Report the malaria status of this cell.
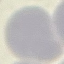

It is uninfected.

Summary:
  - Image type: automatically extracted cell patch, resized to 64 × 64 pixels
  - Preparation: thin blood film
  - Capture: smartphone through the microscope eyepiece
  - Stain: Giemsa